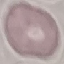

Result: no malaria parasites detected. Automatically extracted cell patch, resized to 64 × 64 pixels. Giemsa stain. Thin blood smear. Photographed with a smartphone camera at the microscope eyepiece.